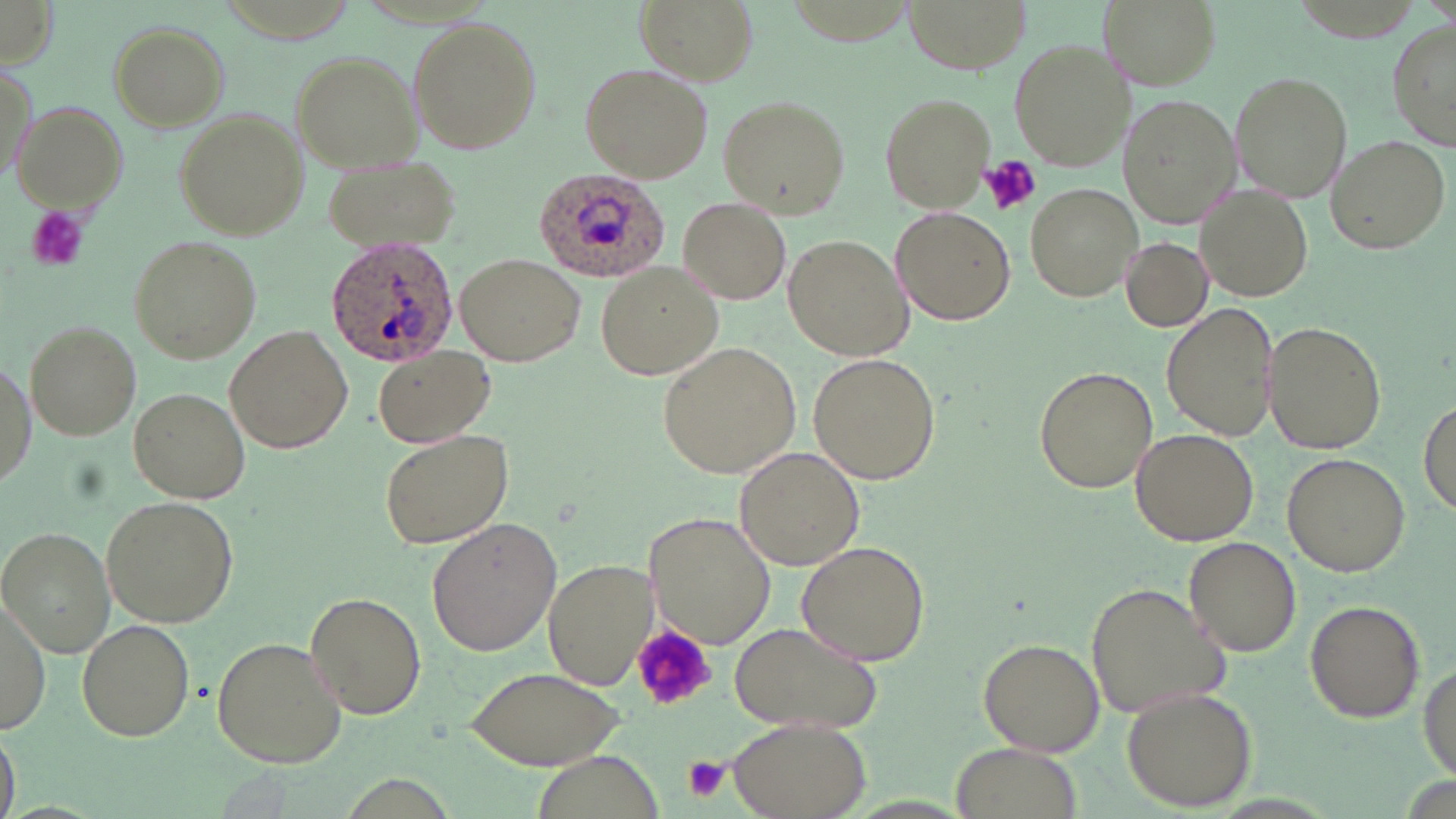
Approximate bounding boxes as named x1/y1/x2/y2 corners in pixels. Uninfected red blood cell locations: (x1=0, y1=0, x2=58, y2=68), (x1=634, y1=0, x2=759, y2=87), (x1=903, y1=0, x2=1029, y2=72), (x1=1101, y1=0, x2=1219, y2=89), (x1=406, y1=17, x2=541, y2=154), (x1=107, y1=20, x2=230, y2=131), (x1=1387, y1=21, x2=1455, y2=153), (x1=1006, y1=38, x2=1130, y2=170), (x1=288, y1=50, x2=422, y2=173), (x1=1, y1=61, x2=38, y2=190), (x1=579, y1=62, x2=713, y2=183), (x1=1229, y1=70, x2=1352, y2=202), (x1=878, y1=92, x2=994, y2=213), (x1=717, y1=94, x2=851, y2=219), (x1=1120, y1=96, x2=1240, y2=230), (x1=15, y1=100, x2=128, y2=211), (x1=175, y1=109, x2=308, y2=240), (x1=1324, y1=132, x2=1452, y2=255), (x1=322, y1=152, x2=458, y2=257), (x1=1027, y1=183, x2=1141, y2=300), (x1=1197, y1=186, x2=1312, y2=299), (x1=678, y1=197, x2=791, y2=306), (x1=894, y1=206, x2=1017, y2=326), (x1=783, y1=232, x2=916, y2=361), (x1=127, y1=235, x2=261, y2=364), (x1=1120, y1=236, x2=1213, y2=332), (x1=455, y1=254, x2=585, y2=367), (x1=594, y1=261, x2=726, y2=381), (x1=1161, y1=303, x2=1280, y2=442), (x1=23, y1=320, x2=142, y2=442), (x1=1262, y1=320, x2=1388, y2=454), (x1=223, y1=325, x2=353, y2=452), (x1=658, y1=342, x2=804, y2=478), (x1=373, y1=344, x2=494, y2=448), (x1=808, y1=351, x2=942, y2=484), (x1=0, y1=355, x2=34, y2=491), (x1=1034, y1=366, x2=1159, y2=495), (x1=129, y1=386, x2=253, y2=503), (x1=1418, y1=395, x2=1454, y2=520), (x1=380, y1=427, x2=515, y2=548), (x1=1130, y1=428, x2=1258, y2=546), (x1=734, y1=445, x2=866, y2=571), (x1=1281, y1=452, x2=1409, y2=577), (x1=101, y1=495, x2=238, y2=627), (x1=648, y1=512, x2=776, y2=649), (x1=428, y1=518, x2=562, y2=657), (x1=1, y1=529, x2=114, y2=655), (x1=1185, y1=538, x2=1303, y2=656), (x1=797, y1=539, x2=930, y2=663), (x1=541, y1=559, x2=657, y2=693), (x1=1088, y1=581, x2=1230, y2=719), (x1=0, y1=589, x2=50, y2=733), (x1=304, y1=591, x2=426, y2=719), (x1=1304, y1=600, x2=1425, y2=722), (x1=78, y1=617, x2=196, y2=741), (x1=728, y1=621, x2=883, y2=733), (x1=212, y1=635, x2=347, y2=768), (x1=976, y1=636, x2=1104, y2=757), (x1=1418, y1=659, x2=1454, y2=781), (x1=464, y1=667, x2=630, y2=770), (x1=1122, y1=686, x2=1258, y2=810), (x1=725, y1=717, x2=872, y2=819), (x1=0, y1=724, x2=21, y2=819), (x1=947, y1=743, x2=1085, y2=819). Platelet locations: (x1=979, y1=155, x2=1040, y2=217), (x1=24, y1=205, x2=90, y2=272), (x1=630, y1=624, x2=718, y2=714), (x1=683, y1=756, x2=730, y2=801). Plasmodium ovale-infected red blood cell locations: (x1=535, y1=167, x2=667, y2=280), (x1=325, y1=235, x2=459, y2=367). Slide-level diagnosis: Plasmodium ovale. Image is 1456×819 pixels. Thin blood film. Optical microscopy. One field of a larger specimen. May-Grünwald-Giemsa-stained preparation. Captured at 1000x magnification.